State which parasite is depicted.
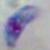
Toxoplasma gondii.

Summary:
  - Modality: photomicrograph
  - Magnification: 1000x